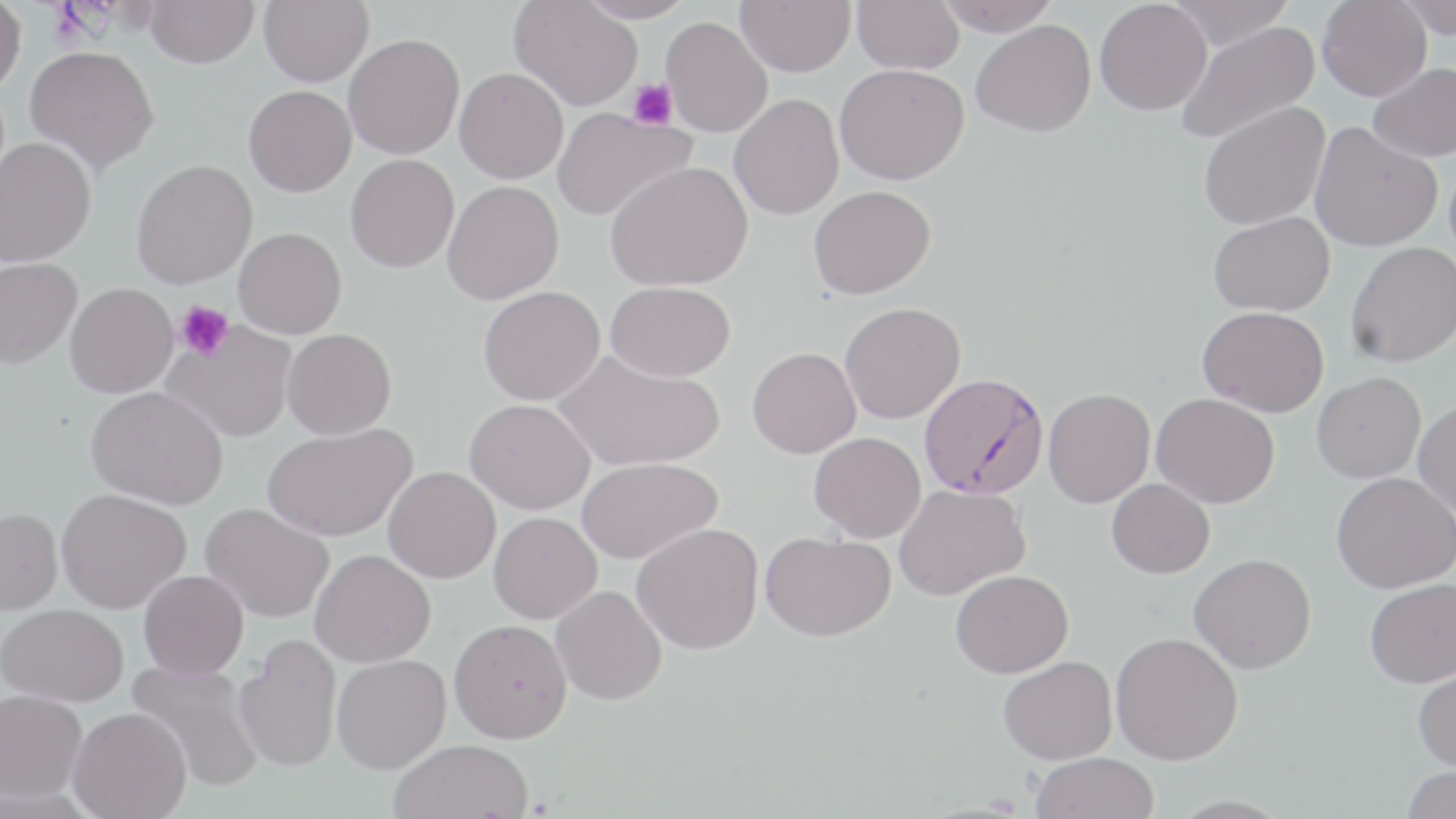
slide-level diagnosis = Plasmodium falciparum
field of view = one of a larger specimen
preparation = thin blood film
modality = optical microscopy
image size = 1456×819 pixels
Plasmodium falciparum-infected red blood cell locations = approximate bounding boxes as [x1, y1, x2, y2] in pixels: [918, 372, 1050, 500]
uninfected red blood cell locations = approximate bounding boxes as [x1, y1, x2, y2] in pixels: [144, 0, 259, 68], [258, 0, 373, 86], [576, 0, 696, 23], [735, 0, 856, 76], [852, 0, 964, 74], [934, 0, 1061, 36], [1094, 0, 1212, 115], [1166, 0, 1295, 50], [1317, 0, 1432, 101], [0, 1, 26, 94], [510, 1, 642, 111], [1393, 1, 1456, 39], [661, 16, 772, 136], [971, 20, 1096, 137], [1176, 20, 1321, 145], [343, 33, 464, 159], [24, 45, 158, 173], [1367, 63, 1456, 162], [835, 64, 969, 185], [454, 67, 568, 184], [243, 85, 356, 197], [729, 94, 844, 220], [1198, 101, 1330, 231], [552, 108, 693, 222], [1310, 121, 1443, 251], [0, 137, 96, 267], [345, 154, 459, 272], [131, 159, 257, 289], [605, 162, 753, 291], [442, 181, 564, 304], [808, 185, 935, 299], [1208, 212, 1334, 316], [233, 227, 347, 339], [1345, 242, 1456, 367], [0, 257, 82, 368], [604, 281, 734, 381], [65, 282, 178, 398], [478, 285, 605, 406], [840, 302, 965, 424], [1198, 306, 1329, 417], [163, 323, 297, 443], [281, 328, 396, 440], [747, 346, 861, 458], [553, 349, 724, 472], [1312, 372, 1426, 483], [86, 385, 228, 509], [1043, 388, 1155, 508], [1151, 393, 1280, 508], [465, 398, 595, 513], [1413, 400, 1456, 521], [262, 422, 417, 541], [809, 432, 926, 542], [576, 457, 722, 565], [382, 466, 500, 583], [1331, 472, 1456, 593], [1107, 478, 1214, 578], [894, 484, 1030, 601], [56, 488, 191, 613], [200, 503, 333, 622], [0, 508, 63, 614], [488, 512, 602, 623], [632, 523, 763, 654], [761, 531, 896, 641], [310, 549, 435, 667], [1189, 553, 1316, 673], [138, 569, 249, 680], [950, 570, 1073, 678], [1365, 578, 1456, 688], [551, 585, 667, 705], [1, 603, 128, 705], [449, 618, 572, 743], [1110, 631, 1243, 765], [234, 636, 342, 773], [332, 654, 451, 773], [999, 655, 1117, 764], [128, 659, 266, 792], [1412, 663, 1456, 772], [0, 689, 87, 802], [68, 707, 191, 818], [389, 739, 534, 819], [1031, 752, 1159, 819], [1401, 765, 1456, 819]
platelet locations = approximate bounding boxes as [x1, y1, x2, y2] in pixels: [627, 78, 677, 131], [175, 300, 234, 361]
stain = May-Grünwald-Giemsa
magnification = 1000x